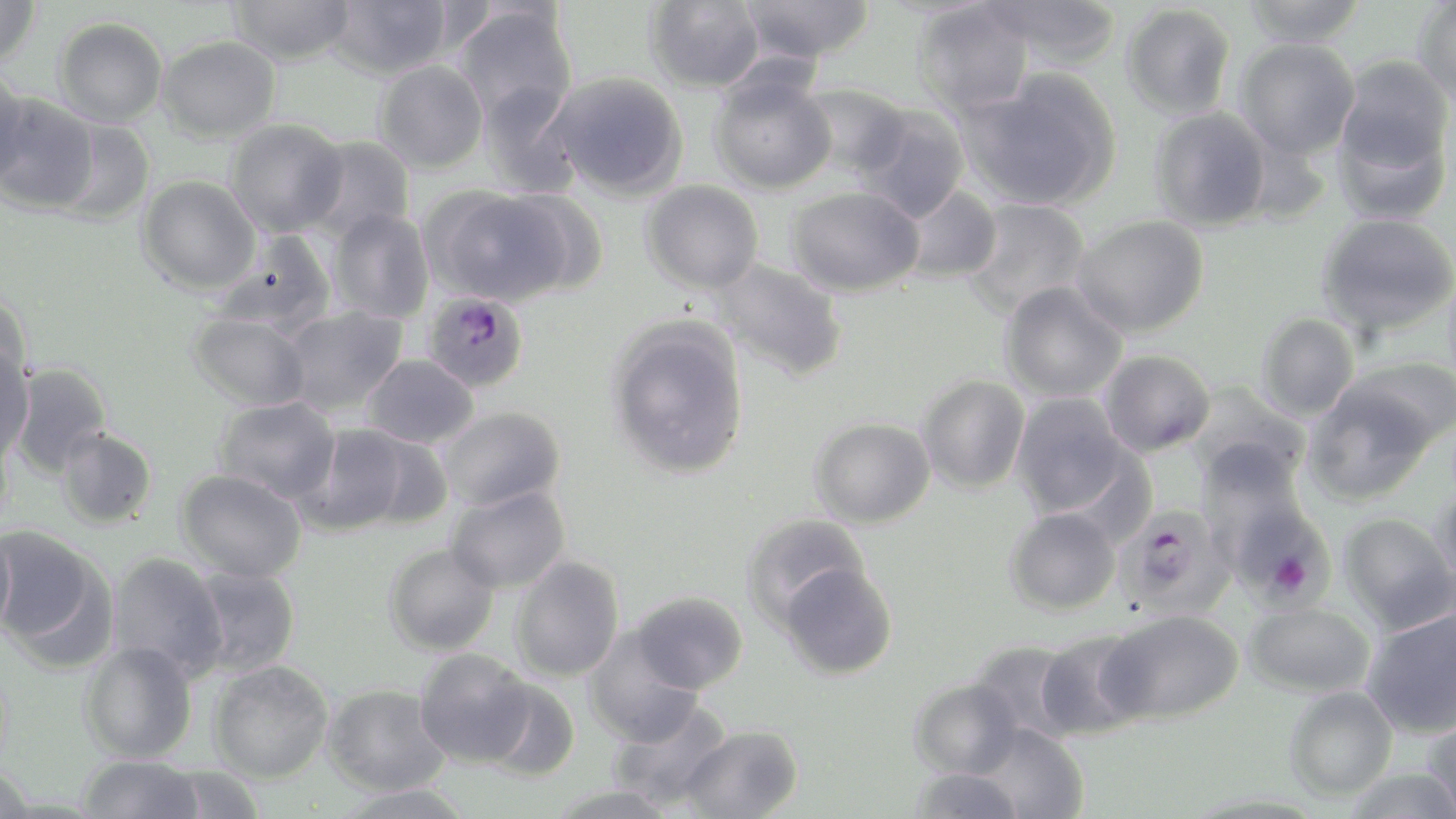
Summary:
  - Coordinate format: approximate bounding boxes as named x1/y1/x2/y2 corners in pixels
  - Uninfected red blood cell locations: (x1=0, y1=0, x2=40, y2=67), (x1=228, y1=0, x2=355, y2=66), (x1=326, y1=0, x2=454, y2=79), (x1=646, y1=0, x2=765, y2=93), (x1=738, y1=0, x2=874, y2=64), (x1=978, y1=0, x2=1123, y2=69), (x1=1242, y1=0, x2=1368, y2=47), (x1=1413, y1=0, x2=1456, y2=105), (x1=912, y1=2, x2=1034, y2=118), (x1=1121, y1=3, x2=1236, y2=121), (x1=453, y1=4, x2=578, y2=127), (x1=54, y1=16, x2=168, y2=127), (x1=157, y1=35, x2=280, y2=143), (x1=1235, y1=38, x2=1360, y2=159), (x1=1334, y1=54, x2=1453, y2=181), (x1=374, y1=60, x2=488, y2=174), (x1=0, y1=67, x2=29, y2=183), (x1=961, y1=70, x2=1121, y2=211), (x1=548, y1=72, x2=687, y2=200), (x1=709, y1=72, x2=837, y2=194), (x1=478, y1=82, x2=583, y2=198), (x1=796, y1=82, x2=910, y2=179), (x1=1, y1=93, x2=101, y2=214), (x1=855, y1=104, x2=970, y2=222), (x1=1150, y1=107, x2=1272, y2=231), (x1=1332, y1=108, x2=1452, y2=226), (x1=52, y1=119, x2=156, y2=225), (x1=225, y1=119, x2=349, y2=237), (x1=304, y1=135, x2=415, y2=243), (x1=137, y1=175, x2=260, y2=295), (x1=641, y1=180, x2=763, y2=294), (x1=897, y1=185, x2=1002, y2=284), (x1=425, y1=186, x2=577, y2=306), (x1=787, y1=186, x2=924, y2=297), (x1=960, y1=199, x2=1091, y2=319), (x1=328, y1=209, x2=434, y2=323), (x1=1317, y1=212, x2=1456, y2=337), (x1=1072, y1=215, x2=1210, y2=337), (x1=211, y1=233, x2=337, y2=335), (x1=712, y1=259, x2=849, y2=382), (x1=999, y1=281, x2=1127, y2=403), (x1=0, y1=293, x2=33, y2=389), (x1=281, y1=306, x2=407, y2=416), (x1=188, y1=310, x2=312, y2=412), (x1=1256, y1=312, x2=1360, y2=421), (x1=606, y1=317, x2=751, y2=480), (x1=0, y1=344, x2=34, y2=460), (x1=1099, y1=350, x2=1215, y2=457), (x1=362, y1=354, x2=478, y2=448), (x1=1343, y1=356, x2=1456, y2=449), (x1=9, y1=361, x2=113, y2=478), (x1=916, y1=375, x2=1030, y2=494), (x1=1303, y1=382, x2=1437, y2=506), (x1=1186, y1=383, x2=1312, y2=490), (x1=1010, y1=394, x2=1131, y2=518), (x1=212, y1=397, x2=340, y2=504), (x1=437, y1=406, x2=566, y2=511), (x1=809, y1=416, x2=935, y2=528), (x1=297, y1=423, x2=416, y2=536), (x1=0, y1=426, x2=13, y2=537), (x1=56, y1=427, x2=157, y2=529), (x1=346, y1=430, x2=454, y2=531), (x1=1197, y1=440, x2=1311, y2=563), (x1=175, y1=468, x2=307, y2=582), (x1=1434, y1=483, x2=1456, y2=593), (x1=446, y1=485, x2=571, y2=594), (x1=1004, y1=507, x2=1120, y2=616), (x1=1339, y1=512, x2=1456, y2=634), (x1=741, y1=513, x2=870, y2=629), (x1=0, y1=524, x2=16, y2=640), (x1=0, y1=527, x2=112, y2=664), (x1=383, y1=543, x2=499, y2=656), (x1=107, y1=551, x2=228, y2=680), (x1=509, y1=555, x2=624, y2=683), (x1=779, y1=561, x2=899, y2=680), (x1=187, y1=565, x2=301, y2=678), (x1=629, y1=591, x2=748, y2=694), (x1=1244, y1=602, x2=1376, y2=698), (x1=1361, y1=606, x2=1456, y2=739), (x1=1099, y1=609, x2=1244, y2=725), (x1=583, y1=629, x2=702, y2=746), (x1=1033, y1=629, x2=1149, y2=741), (x1=969, y1=640, x2=1083, y2=744), (x1=79, y1=641, x2=197, y2=763), (x1=413, y1=648, x2=534, y2=767), (x1=209, y1=660, x2=333, y2=784), (x1=909, y1=677, x2=1023, y2=779), (x1=482, y1=679, x2=580, y2=781), (x1=323, y1=684, x2=451, y2=796), (x1=1284, y1=686, x2=1397, y2=801), (x1=607, y1=698, x2=733, y2=811), (x1=1423, y1=709, x2=1456, y2=818), (x1=681, y1=724, x2=803, y2=818), (x1=972, y1=724, x2=1088, y2=818), (x1=77, y1=754, x2=206, y2=819), (x1=0, y1=762, x2=37, y2=818), (x1=161, y1=765, x2=266, y2=819), (x1=906, y1=766, x2=1027, y2=818), (x1=545, y1=782, x2=680, y2=819), (x1=332, y1=783, x2=477, y2=819)
  - Plasmodium falciparum-infected red blood cell locations: (x1=422, y1=291, x2=529, y2=393), (x1=1228, y1=494, x2=1335, y2=608), (x1=1117, y1=503, x2=1235, y2=621)
  - Slide-level diagnosis: Plasmodium falciparum
  - Magnification: 1000x
  - Modality: light microscopy
  - Preparation: thin blood film
  - Image size: 1456×819 pixels
  - Stain: May-Grünwald-Giemsa
  - Field of view: one of a larger specimen